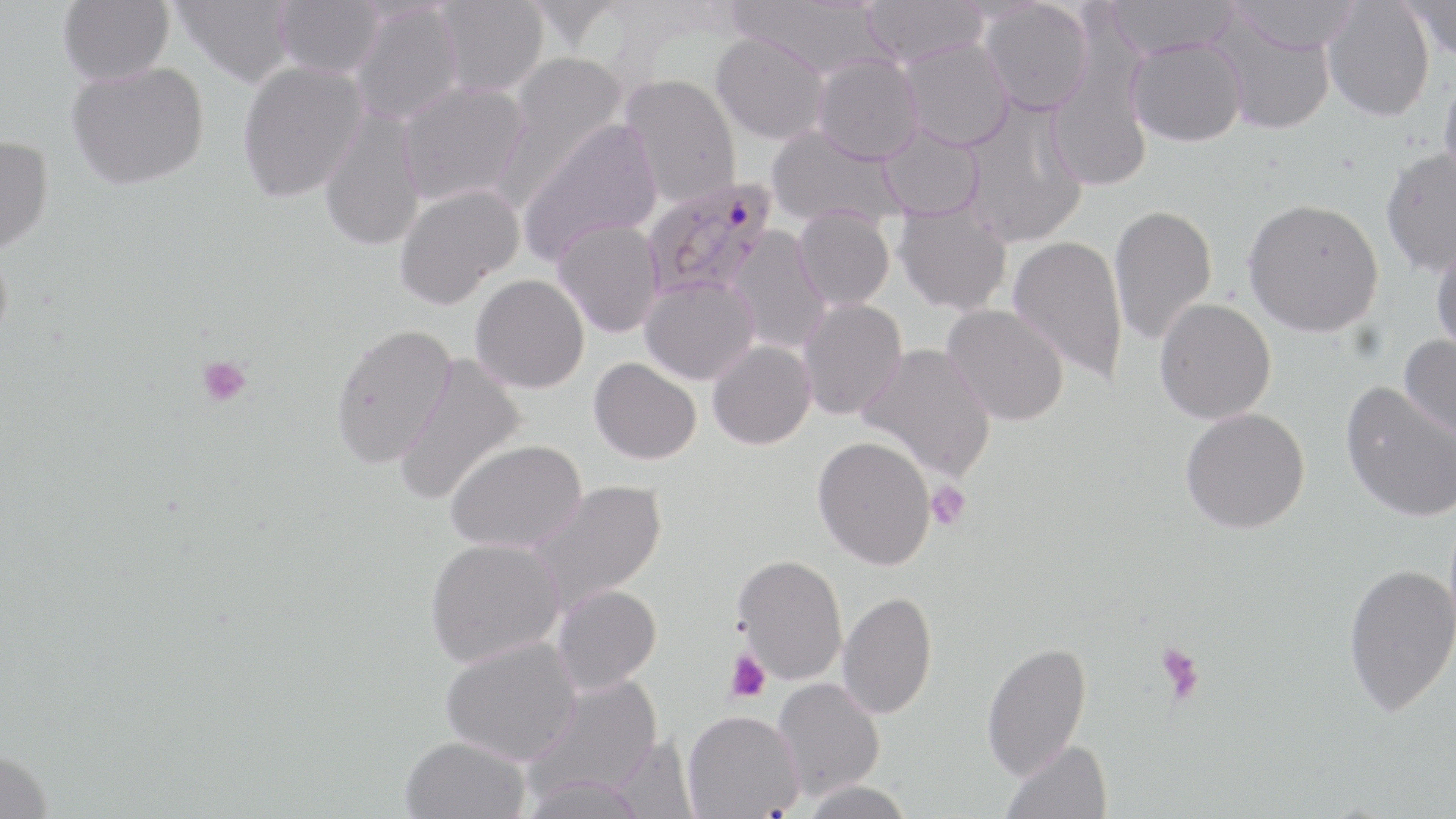
Summary:
  - Coordinate format: approximate bounding boxes as named x1/y1/x2/y2 corners in pixels
  - Plasmodium falciparum-infected red blood cell locations: (x1=643, y1=175, x2=779, y2=302)
  - Platelet locations: (x1=196, y1=354, x2=253, y2=409), (x1=926, y1=480, x2=971, y2=530), (x1=1154, y1=641, x2=1205, y2=703), (x1=726, y1=648, x2=771, y2=704)
  - Uninfected red blood cell locations: (x1=58, y1=0, x2=175, y2=87), (x1=173, y1=0, x2=295, y2=87), (x1=273, y1=0, x2=385, y2=79), (x1=435, y1=0, x2=548, y2=97), (x1=729, y1=0, x2=892, y2=80), (x1=864, y1=0, x2=989, y2=66), (x1=1102, y1=0, x2=1240, y2=59), (x1=1226, y1=0, x2=1363, y2=55), (x1=1400, y1=0, x2=1456, y2=63), (x1=979, y1=1, x2=1093, y2=115), (x1=1322, y1=1, x2=1435, y2=122), (x1=350, y1=4, x2=462, y2=125), (x1=1208, y1=13, x2=1338, y2=135), (x1=711, y1=31, x2=829, y2=145), (x1=1126, y1=36, x2=1247, y2=147), (x1=899, y1=38, x2=1014, y2=151), (x1=498, y1=51, x2=629, y2=194), (x1=813, y1=54, x2=924, y2=164), (x1=237, y1=61, x2=368, y2=203), (x1=67, y1=63, x2=210, y2=193), (x1=1439, y1=63, x2=1456, y2=195), (x1=620, y1=73, x2=741, y2=207), (x1=398, y1=80, x2=531, y2=206), (x1=959, y1=97, x2=1089, y2=248), (x1=318, y1=107, x2=426, y2=252), (x1=517, y1=118, x2=663, y2=265), (x1=877, y1=123, x2=986, y2=221), (x1=766, y1=124, x2=905, y2=230), (x1=0, y1=137, x2=55, y2=260), (x1=1379, y1=146, x2=1456, y2=278), (x1=395, y1=183, x2=524, y2=309), (x1=1243, y1=197, x2=1385, y2=338), (x1=894, y1=202, x2=1013, y2=316), (x1=1108, y1=204, x2=1218, y2=346), (x1=793, y1=206, x2=895, y2=311), (x1=553, y1=218, x2=664, y2=338), (x1=725, y1=226, x2=831, y2=355), (x1=1007, y1=235, x2=1128, y2=384), (x1=1430, y1=241, x2=1456, y2=360), (x1=471, y1=274, x2=590, y2=393), (x1=640, y1=276, x2=760, y2=385), (x1=798, y1=298, x2=908, y2=421), (x1=1154, y1=298, x2=1276, y2=425), (x1=941, y1=303, x2=1070, y2=427), (x1=331, y1=322, x2=457, y2=470), (x1=1399, y1=335, x2=1456, y2=448), (x1=707, y1=339, x2=817, y2=449), (x1=856, y1=342, x2=997, y2=482), (x1=394, y1=353, x2=527, y2=506), (x1=589, y1=357, x2=702, y2=464), (x1=1339, y1=381, x2=1455, y2=522), (x1=1180, y1=407, x2=1310, y2=534), (x1=812, y1=435, x2=937, y2=570), (x1=446, y1=438, x2=586, y2=553), (x1=526, y1=479, x2=668, y2=615), (x1=425, y1=537, x2=565, y2=668), (x1=733, y1=554, x2=848, y2=685), (x1=1342, y1=563, x2=1456, y2=717), (x1=552, y1=584, x2=662, y2=695), (x1=837, y1=590, x2=937, y2=720), (x1=440, y1=636, x2=583, y2=766), (x1=981, y1=641, x2=1092, y2=780), (x1=525, y1=675, x2=664, y2=802), (x1=772, y1=677, x2=885, y2=801), (x1=683, y1=710, x2=803, y2=818), (x1=400, y1=735, x2=531, y2=819), (x1=609, y1=735, x2=699, y2=819), (x1=1001, y1=739, x2=1113, y2=819), (x1=0, y1=752, x2=54, y2=819), (x1=520, y1=773, x2=648, y2=819), (x1=802, y1=779, x2=914, y2=819)
  - Slide-level diagnosis: Plasmodium falciparum
  - Field of view: single
  - Stain: May-Grünwald-Giemsa
  - Modality: optical microscopy
  - Image size: 1456×819 pixels
  - Magnification: 1000x
  - Preparation: thin blood film